Classify this cell by malaria status.
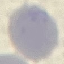

Uninfected.

Acquired by smartphone through the microscope eyepiece. Thin smear of blood. Cell patch, automatically extracted from a larger field of view and resized to 64 × 64 pixels. Giemsa stain.